Locate every blood parasite and identify its species.
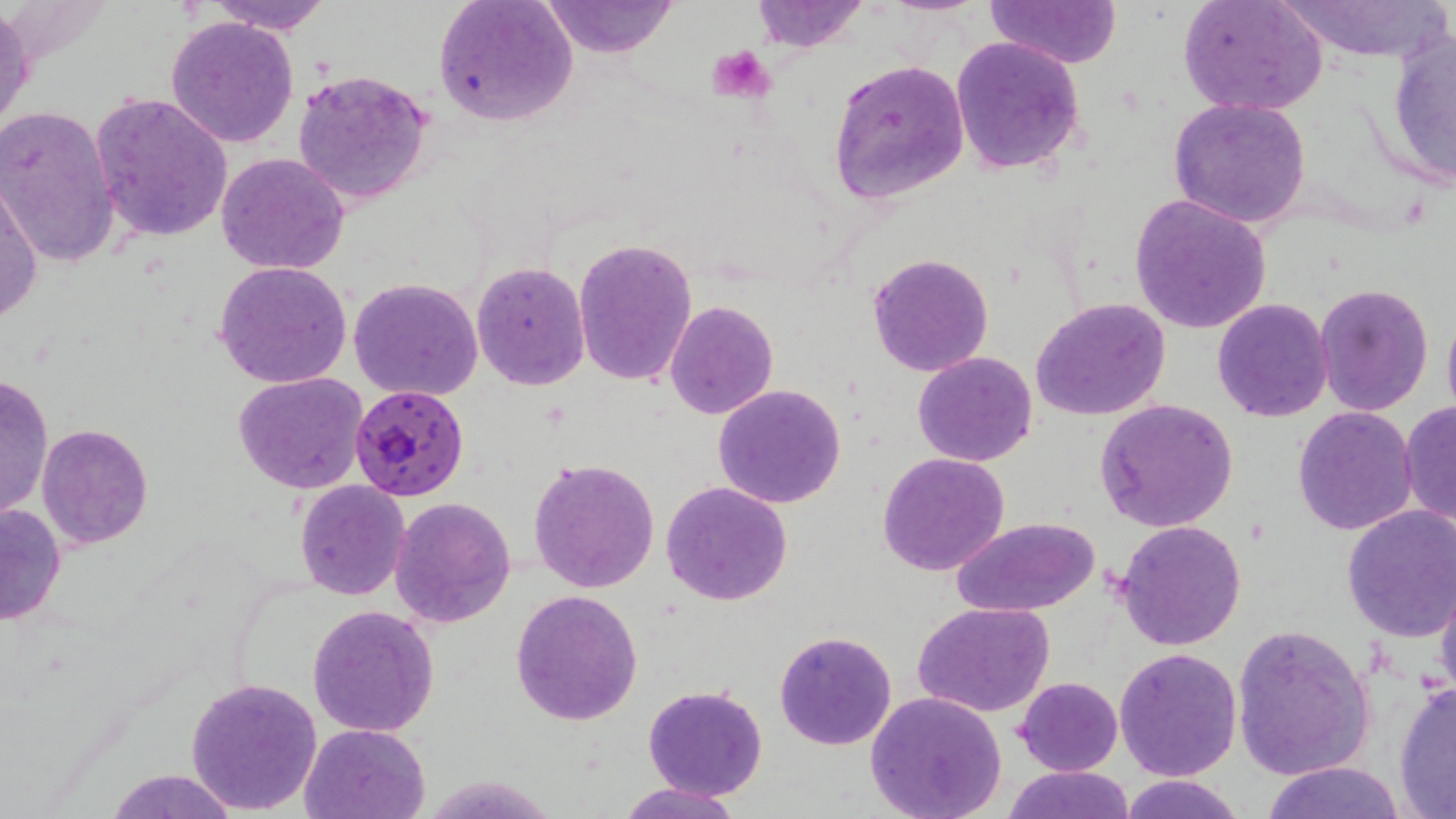

Approximate bounding boxes as [x1, y1, x2, y2] in pixels.
Plasmodium falciparum-infected red blood cells: [349, 383, 471, 500].
No Plasmodium ovale, Plasmodium malariae, Plasmodium vivax, Babesia divergens, or Trypanosoma brucei observed.

{
  "slide_level_diagnosis": "Plasmodium falciparum",
  "magnification": "1000x",
  "uninfected_red_blood_cell_locations": "approximate bounding boxes as [x1, y1, x2, y2] in pixels: [207, 0, 332, 36], [541, 0, 680, 56], [751, 0, 868, 53], [880, 0, 988, 16], [986, 0, 1121, 68], [1178, 0, 1327, 117], [1273, 0, 1451, 64], [433, 1, 579, 128], [1, 3, 34, 142], [165, 15, 299, 148], [1384, 30, 1456, 190], [951, 37, 1088, 176], [827, 59, 968, 203], [291, 67, 434, 207], [90, 91, 232, 241], [1168, 97, 1313, 229], [0, 105, 120, 270], [214, 153, 351, 276], [0, 181, 44, 323], [1130, 195, 1272, 334], [572, 237, 698, 386], [866, 251, 994, 377], [213, 261, 353, 387], [471, 261, 592, 392], [349, 277, 483, 401], [1314, 282, 1434, 416], [1031, 298, 1172, 422], [1212, 298, 1332, 423], [665, 301, 779, 419], [1442, 304, 1456, 428], [913, 351, 1037, 466], [0, 372, 53, 522], [232, 372, 369, 494], [712, 384, 847, 508], [1094, 398, 1239, 531], [1398, 398, 1456, 531], [1292, 407, 1418, 535], [37, 424, 153, 549], [876, 452, 1010, 576], [527, 457, 660, 595], [295, 481, 411, 601], [661, 481, 793, 606], [389, 496, 517, 629], [0, 503, 66, 626], [1341, 506, 1456, 640], [953, 516, 1099, 618], [1115, 519, 1247, 652], [1433, 573, 1456, 700], [510, 589, 644, 725], [912, 603, 1056, 718], [307, 604, 440, 737], [1230, 625, 1373, 780], [773, 630, 897, 751], [1114, 646, 1242, 781], [185, 676, 323, 815], [1016, 677, 1123, 776], [1392, 681, 1456, 817], [642, 683, 769, 801], [863, 692, 1007, 819], [299, 724, 431, 819], [1260, 762, 1408, 819], [1002, 766, 1132, 819], [105, 769, 235, 818], [1118, 774, 1248, 818], [618, 782, 740, 819]",
  "field_of_view": "one of a larger specimen",
  "preparation": "thin blood film",
  "stain": "May-Grünwald-Giemsa",
  "platelet_locations": "approximate bounding boxes as [x1, y1, x2, y2] in pixels: [708, 45, 778, 103]",
  "image_size": "1456×819 pixels",
  "modality": "light microscopy"
}